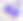

Summary:
  - Magnification: 400x
  - Identification: Toxoplasma gondii
  - Modality: photomicrograph